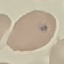
Malaria status: uninfected. Acquired by smartphone through the microscope eyepiece. Giemsa stain. Cell patch, automatically extracted from a larger field of view and resized to 64 × 64 pixels. Thin smear of blood.